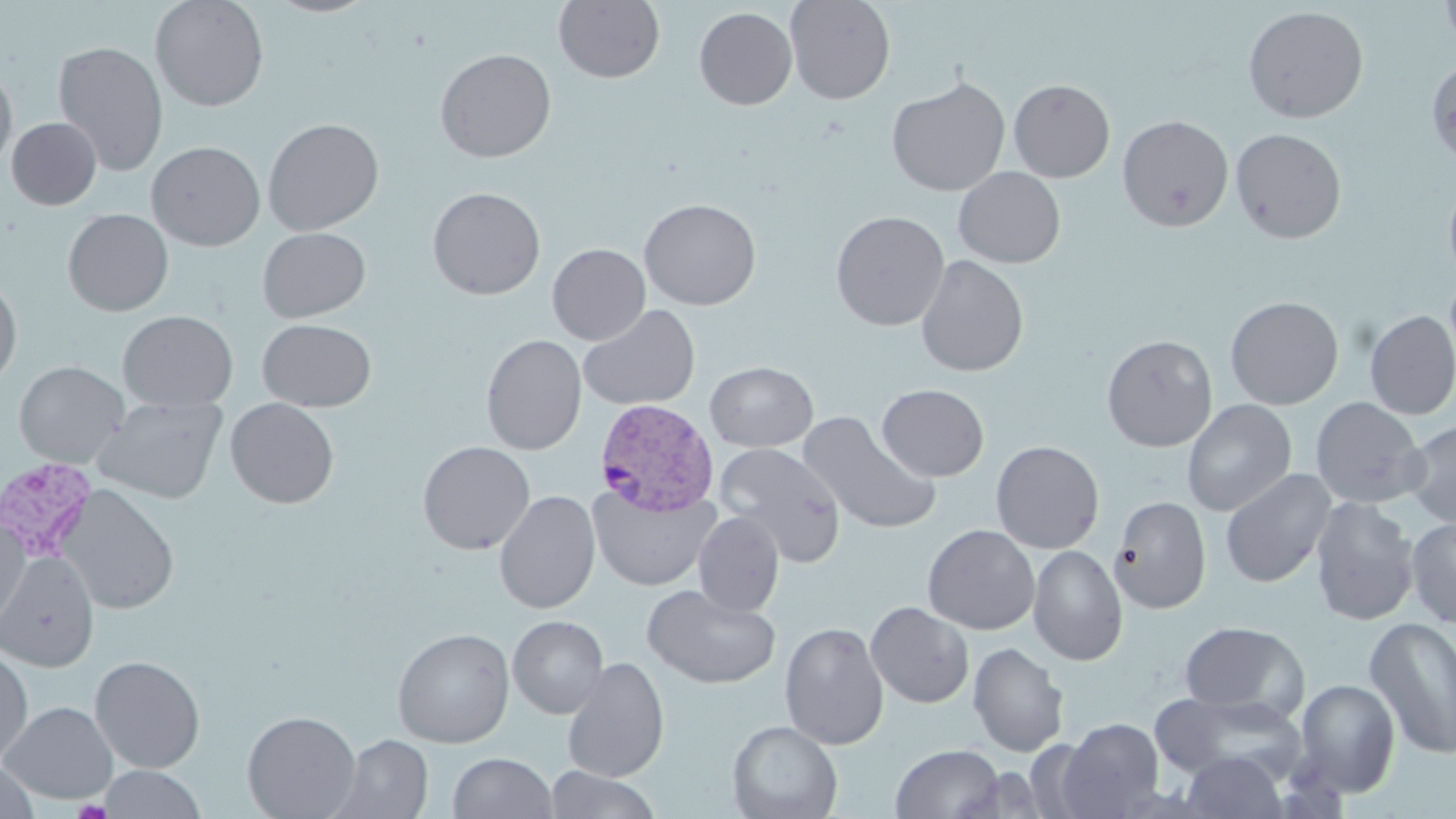
slide-level diagnosis = Plasmodium vivax
stain = May-Grünwald-Giemsa
field of view = one of a larger specimen
magnification = 1000x
Plasmodium vivax-infected red blood cell locations = approximate bounding boxes as (x1, y1, x2, y2) in pixels: (595, 399, 720, 516), (0, 458, 104, 564)
uninfected red blood cell locations = approximate bounding boxes as (x1, y1, x2, y2) in pixels: (149, 0, 269, 112), (263, 0, 379, 18), (553, 0, 665, 83), (785, 0, 896, 105), (1440, 0, 1456, 54), (1242, 5, 1369, 123), (694, 7, 798, 110), (52, 40, 169, 176), (434, 48, 557, 163), (1425, 59, 1456, 167), (0, 60, 18, 173), (886, 76, 1010, 197), (1008, 78, 1115, 182), (1117, 115, 1234, 232), (7, 117, 101, 210), (263, 117, 385, 235), (1230, 127, 1347, 244), (146, 141, 266, 251), (953, 167, 1066, 268), (1442, 173, 1456, 285), (427, 187, 546, 300), (638, 198, 762, 310), (62, 209, 174, 317), (829, 210, 950, 331), (257, 226, 370, 323), (547, 243, 651, 345), (915, 254, 1029, 377), (0, 277, 23, 392), (1225, 296, 1344, 410), (578, 304, 701, 412), (118, 310, 238, 411), (1364, 311, 1456, 420), (257, 318, 376, 412), (480, 333, 587, 455), (1101, 334, 1218, 452), (13, 361, 129, 468), (704, 361, 818, 452), (876, 384, 989, 482), (91, 396, 228, 505), (1310, 397, 1428, 508), (225, 398, 340, 509), (1181, 399, 1297, 517), (798, 411, 941, 536), (1403, 418, 1456, 529), (417, 440, 535, 555), (991, 440, 1105, 554), (714, 443, 847, 566), (1220, 469, 1337, 588), (588, 484, 719, 591), (57, 485, 179, 615), (494, 490, 601, 614), (1109, 496, 1211, 614), (1309, 496, 1419, 626), (693, 511, 784, 617), (1405, 518, 1456, 628), (0, 519, 30, 630), (922, 524, 1040, 635), (1027, 544, 1128, 665), (0, 552, 100, 674), (641, 583, 782, 689), (865, 602, 975, 708), (507, 615, 609, 719), (1364, 616, 1456, 760), (1179, 620, 1308, 719), (779, 621, 889, 750), (392, 627, 514, 748), (968, 642, 1069, 757), (0, 648, 33, 769), (89, 655, 206, 773), (562, 657, 669, 783), (1292, 678, 1401, 797), (1151, 692, 1305, 783), (1, 701, 118, 804), (242, 710, 361, 819), (1058, 718, 1164, 818), (727, 720, 843, 819), (330, 734, 433, 819), (891, 744, 1005, 819), (1178, 751, 1287, 818), (447, 752, 558, 818), (0, 762, 39, 818), (99, 765, 207, 819), (545, 767, 663, 819)
modality = light microscopy
preparation = thin blood smear
image size = 1456×819 pixels